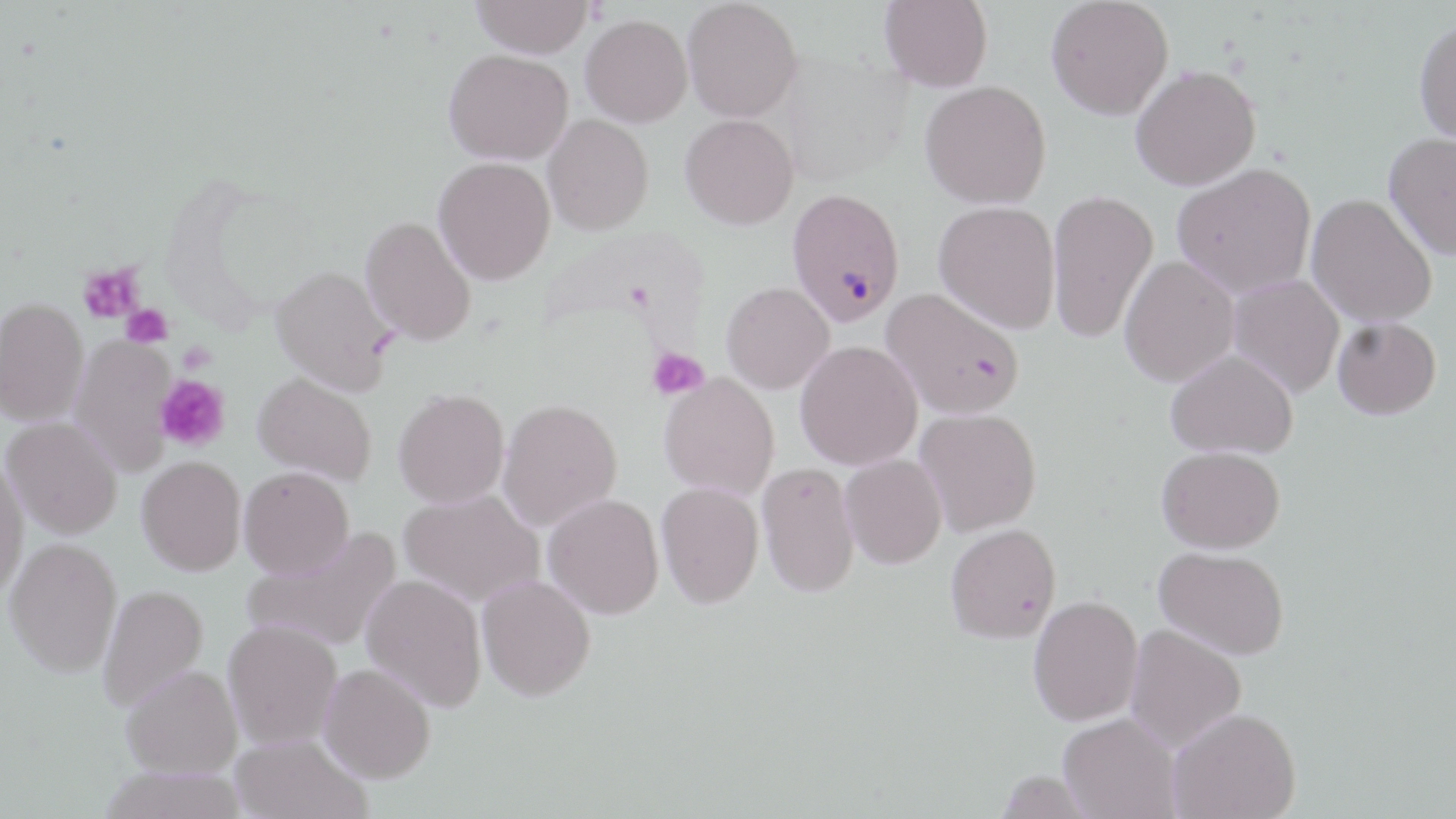

Plasmodium falciparum-infected red blood cell locations = approximate bounding boxes as named x1/y1/x2/y2 corners in pixels: (x1=787, y1=194, x2=906, y2=332)
slide-level diagnosis = Plasmodium falciparum
uninfected red blood cell locations = approximate bounding boxes as named x1/y1/x2/y2 corners in pixels: (x1=471, y1=0, x2=592, y2=59), (x1=682, y1=0, x2=803, y2=122), (x1=880, y1=0, x2=993, y2=92), (x1=1045, y1=0, x2=1173, y2=120), (x1=581, y1=14, x2=693, y2=127), (x1=1413, y1=16, x2=1456, y2=146), (x1=444, y1=48, x2=573, y2=165), (x1=1131, y1=64, x2=1261, y2=190), (x1=920, y1=80, x2=1052, y2=209), (x1=680, y1=113, x2=799, y2=229), (x1=543, y1=114, x2=654, y2=235), (x1=1383, y1=131, x2=1456, y2=260), (x1=433, y1=157, x2=556, y2=285), (x1=1172, y1=162, x2=1316, y2=297), (x1=1047, y1=189, x2=1159, y2=343), (x1=1307, y1=194, x2=1438, y2=328), (x1=934, y1=200, x2=1060, y2=333), (x1=360, y1=214, x2=477, y2=346), (x1=1120, y1=256, x2=1239, y2=387), (x1=270, y1=264, x2=396, y2=396), (x1=1228, y1=275, x2=1344, y2=398), (x1=722, y1=281, x2=834, y2=393), (x1=881, y1=288, x2=1024, y2=419), (x1=0, y1=297, x2=89, y2=426), (x1=1332, y1=317, x2=1442, y2=420), (x1=69, y1=334, x2=178, y2=476), (x1=795, y1=341, x2=923, y2=470), (x1=1166, y1=349, x2=1298, y2=458), (x1=253, y1=372, x2=377, y2=485), (x1=659, y1=374, x2=780, y2=499), (x1=393, y1=388, x2=509, y2=508), (x1=497, y1=398, x2=622, y2=532), (x1=915, y1=408, x2=1042, y2=536), (x1=2, y1=416, x2=123, y2=538), (x1=1156, y1=445, x2=1285, y2=554), (x1=0, y1=453, x2=28, y2=601), (x1=840, y1=454, x2=946, y2=569), (x1=137, y1=455, x2=246, y2=575), (x1=757, y1=462, x2=860, y2=598), (x1=239, y1=466, x2=354, y2=578), (x1=656, y1=482, x2=764, y2=608), (x1=399, y1=489, x2=543, y2=606), (x1=543, y1=493, x2=664, y2=618), (x1=945, y1=524, x2=1062, y2=644), (x1=245, y1=526, x2=401, y2=652), (x1=5, y1=537, x2=123, y2=677), (x1=1153, y1=545, x2=1290, y2=659), (x1=360, y1=573, x2=488, y2=712), (x1=477, y1=574, x2=596, y2=701), (x1=97, y1=584, x2=208, y2=711), (x1=1028, y1=595, x2=1143, y2=726), (x1=223, y1=619, x2=343, y2=749), (x1=1124, y1=624, x2=1247, y2=752), (x1=318, y1=663, x2=436, y2=783), (x1=121, y1=665, x2=242, y2=778), (x1=1169, y1=707, x2=1300, y2=819), (x1=1058, y1=714, x2=1180, y2=819), (x1=230, y1=733, x2=371, y2=819), (x1=98, y1=766, x2=249, y2=819), (x1=994, y1=770, x2=1098, y2=818)
platelet locations = approximate bounding boxes as named x1/y1/x2/y2 corners in pixels: (x1=77, y1=264, x2=144, y2=323), (x1=121, y1=303, x2=173, y2=348), (x1=177, y1=342, x2=217, y2=375), (x1=646, y1=347, x2=709, y2=400), (x1=155, y1=375, x2=230, y2=452)
stain = May-Grünwald-Giemsa
image size = 1456×819 pixels
field of view = single
magnification = 1000x
modality = light microscopy
preparation = thin blood smear